State which parasite is depicted.
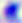

Toxoplasma gondii.

400x magnification. Photomicrograph.